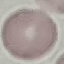

result: negative for malaria parasites
preparation: thin blood film
capture: smartphone camera at the microscope eyepiece
image_type: automatically extracted cell patch, resized to 64 × 64 pixels
stain: Giemsa